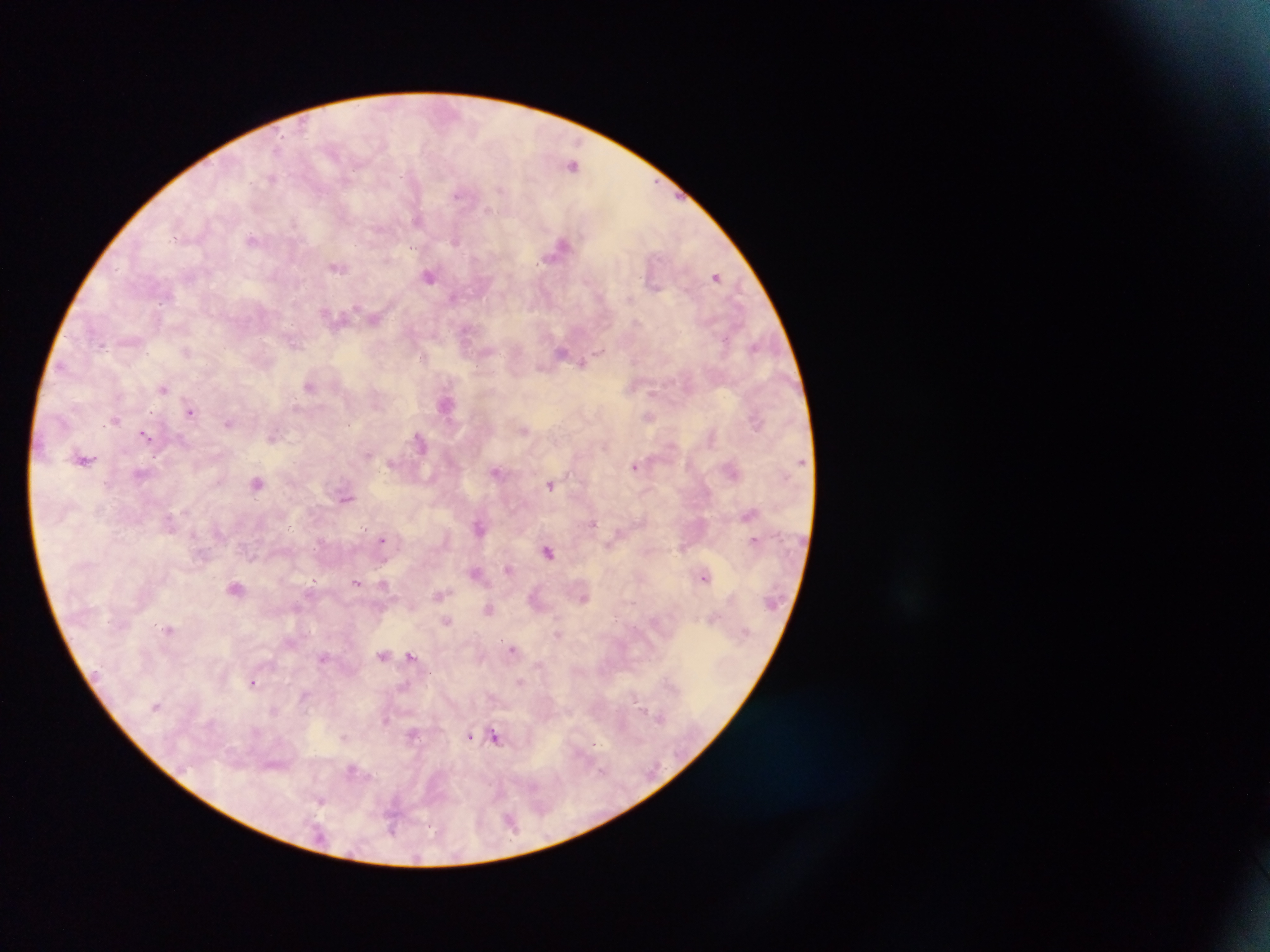

malaria parasite locations = approximate centers as (x, y) in pixels: (277, 149), (572, 165), (271, 178), (501, 189), (457, 194), (486, 210), (418, 220), (293, 223), (252, 240), (457, 241), (561, 244), (387, 259), (338, 268), (429, 276), (716, 276), (453, 298), (630, 298), (356, 306), (325, 311), (374, 320), (635, 321), (102, 344), (295, 344), (756, 345), (600, 351), (562, 352), (424, 357), (582, 363), (310, 386), (164, 388), (651, 392), (190, 411), (151, 412), (649, 416), (115, 420), (229, 423), (523, 430), (144, 435), (272, 437), (419, 441), (85, 459), (635, 466), (496, 472), (257, 483), (551, 485), (346, 497), (593, 523), (478, 526), (365, 527), (382, 539), (754, 539), (548, 552), (507, 568), (476, 572), (704, 577), (356, 582), (313, 583), (384, 583), (236, 588), (438, 595), (584, 598), (489, 608), (447, 621), (168, 630), (513, 649), (383, 654), (411, 655), (323, 656), (519, 681), (253, 682), (635, 701), (156, 706), (659, 717), (386, 719), (413, 733), (470, 735), (344, 737), (496, 737), (594, 744), (352, 769), (602, 770), (322, 800), (392, 827)
field of view = single
leukocyte locations = approximate centers as (x, y) in pixels: (446, 405)
image size = 1270×952 pixels
capture = mobile-phone photograph through a microscope
country = Ghana
preparation = thick blood smear